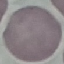
{
  "malaria_status": "uninfected",
  "stain": "Giemsa",
  "image_type": "cell patch, automatically extracted from a larger field of view and resized to 64 × 64 pixels",
  "capture": "smartphone through the microscope eyepiece",
  "preparation": "thin blood film"
}